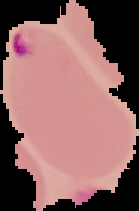

Summary:
  - Malaria status: parasitized
  - Image size: 139×211 pixels
  - Image type: segmented cell region with the area outside set to black
  - Preparation: thin blood smear